Report the malaria status of this cell.
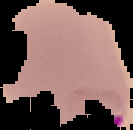

It is parasitized.

image size = 133×130 pixels
image type = segmented cell region on a black background
preparation = thin blood smear